Assess this cell for malaria.
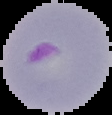
It is parasitized.

Segmented cell region on a black background. Image is 112×115 pixels. From a thin blood film.